Assess this cell for malaria.
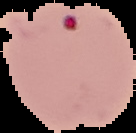

Parasitized.

From a thin blood film. The area outside the segmented cell region is set to black. Image is 136×133 pixels.